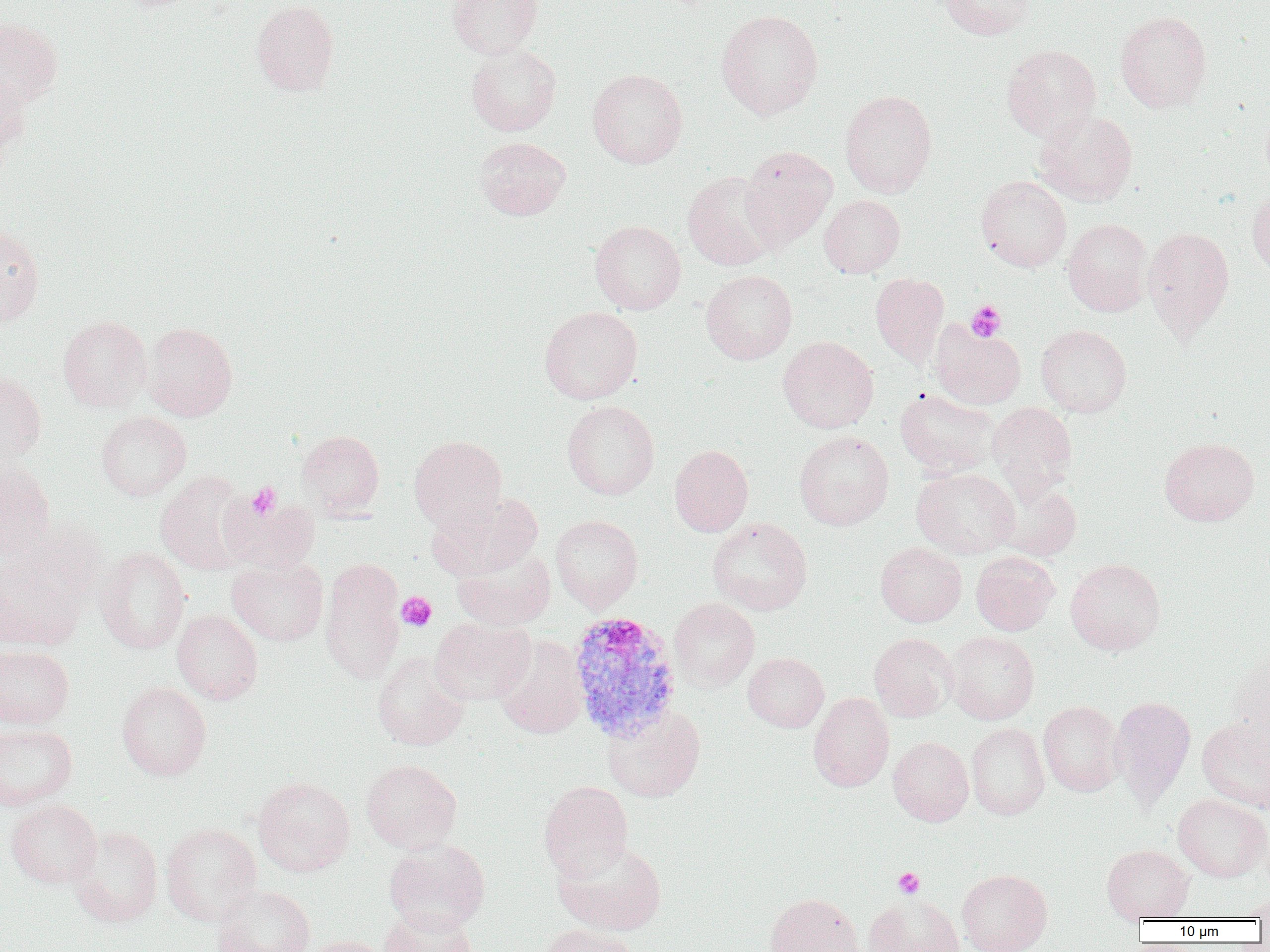

Summary:
  - Coordinate format: approximate bounding boxes as named x1/y1/x2/y2 corners in pixels
  - Uninfected red blood cell locations: (x1=251, y1=0, x2=339, y2=95), (x1=448, y1=0, x2=543, y2=59), (x1=938, y1=0, x2=1036, y2=40), (x1=716, y1=10, x2=823, y2=119), (x1=1115, y1=10, x2=1212, y2=112), (x1=0, y1=18, x2=63, y2=109), (x1=466, y1=44, x2=562, y2=136), (x1=1001, y1=44, x2=1101, y2=141), (x1=588, y1=68, x2=687, y2=168), (x1=1, y1=70, x2=33, y2=169), (x1=839, y1=90, x2=937, y2=197), (x1=1034, y1=109, x2=1138, y2=206), (x1=474, y1=136, x2=571, y2=220), (x1=740, y1=145, x2=836, y2=248), (x1=682, y1=170, x2=783, y2=271), (x1=976, y1=175, x2=1072, y2=271), (x1=1247, y1=187, x2=1270, y2=276), (x1=819, y1=195, x2=905, y2=277), (x1=1063, y1=218, x2=1152, y2=316), (x1=590, y1=220, x2=686, y2=315), (x1=0, y1=226, x2=44, y2=327), (x1=1143, y1=226, x2=1235, y2=338), (x1=701, y1=269, x2=797, y2=364), (x1=870, y1=273, x2=949, y2=366), (x1=539, y1=306, x2=643, y2=404), (x1=58, y1=316, x2=152, y2=411), (x1=930, y1=320, x2=1025, y2=409), (x1=143, y1=322, x2=238, y2=421), (x1=1035, y1=325, x2=1132, y2=416), (x1=777, y1=335, x2=879, y2=433), (x1=0, y1=371, x2=46, y2=464), (x1=895, y1=388, x2=999, y2=478), (x1=562, y1=400, x2=660, y2=499), (x1=987, y1=403, x2=1077, y2=499), (x1=96, y1=411, x2=191, y2=501), (x1=296, y1=430, x2=385, y2=519), (x1=794, y1=430, x2=893, y2=530), (x1=409, y1=435, x2=507, y2=532), (x1=1159, y1=437, x2=1259, y2=526), (x1=669, y1=444, x2=753, y2=536), (x1=0, y1=463, x2=55, y2=559), (x1=911, y1=467, x2=1020, y2=558), (x1=155, y1=471, x2=253, y2=575), (x1=992, y1=479, x2=1081, y2=561), (x1=426, y1=492, x2=542, y2=581), (x1=220, y1=494, x2=320, y2=574), (x1=550, y1=515, x2=643, y2=612), (x1=708, y1=517, x2=812, y2=615), (x1=1, y1=535, x2=92, y2=650), (x1=875, y1=542, x2=966, y2=627), (x1=95, y1=547, x2=190, y2=654), (x1=452, y1=547, x2=555, y2=631), (x1=971, y1=551, x2=1060, y2=635), (x1=227, y1=557, x2=328, y2=646), (x1=320, y1=558, x2=406, y2=684), (x1=1065, y1=558, x2=1166, y2=655), (x1=669, y1=597, x2=759, y2=692), (x1=172, y1=610, x2=263, y2=704), (x1=430, y1=617, x2=535, y2=706), (x1=946, y1=631, x2=1040, y2=724), (x1=869, y1=632, x2=959, y2=721), (x1=494, y1=636, x2=588, y2=739), (x1=0, y1=644, x2=74, y2=729), (x1=1228, y1=646, x2=1270, y2=752), (x1=371, y1=652, x2=471, y2=751), (x1=743, y1=653, x2=829, y2=732), (x1=117, y1=682, x2=212, y2=780), (x1=808, y1=693, x2=894, y2=792), (x1=1110, y1=695, x2=1196, y2=806), (x1=1038, y1=701, x2=1124, y2=796), (x1=602, y1=704, x2=706, y2=802), (x1=1197, y1=717, x2=1270, y2=813), (x1=966, y1=722, x2=1050, y2=820), (x1=0, y1=723, x2=78, y2=810), (x1=888, y1=736, x2=974, y2=826), (x1=361, y1=759, x2=461, y2=853), (x1=253, y1=776, x2=355, y2=876), (x1=538, y1=781, x2=633, y2=881), (x1=1172, y1=794, x2=1270, y2=882), (x1=5, y1=799, x2=102, y2=888), (x1=161, y1=823, x2=262, y2=926), (x1=68, y1=826, x2=163, y2=927), (x1=384, y1=840, x2=490, y2=934), (x1=552, y1=840, x2=667, y2=935), (x1=1101, y1=844, x2=1194, y2=921), (x1=956, y1=868, x2=1052, y2=952), (x1=212, y1=885, x2=315, y2=952), (x1=764, y1=893, x2=863, y2=952), (x1=862, y1=893, x2=964, y2=952), (x1=1241, y1=894, x2=1270, y2=920), (x1=380, y1=908, x2=477, y2=952), (x1=538, y1=924, x2=639, y2=952), (x1=303, y1=935, x2=390, y2=952)
  - Platelet locations: (x1=966, y1=300, x2=1007, y2=341), (x1=247, y1=483, x2=282, y2=519), (x1=396, y1=592, x2=436, y2=632), (x1=893, y1=867, x2=925, y2=898)
  - Plasmodium vivax-infected red blood cell locations: (x1=567, y1=609, x2=683, y2=742)
  - Slide-level diagnosis: Plasmodium vivax
  - Image size: 1270×952 pixels
  - Preparation: thin blood smear
  - Magnification: 1000x
  - Modality: light microscopy
  - Field of view: single